Comment on the morphology of the erythrocytes.
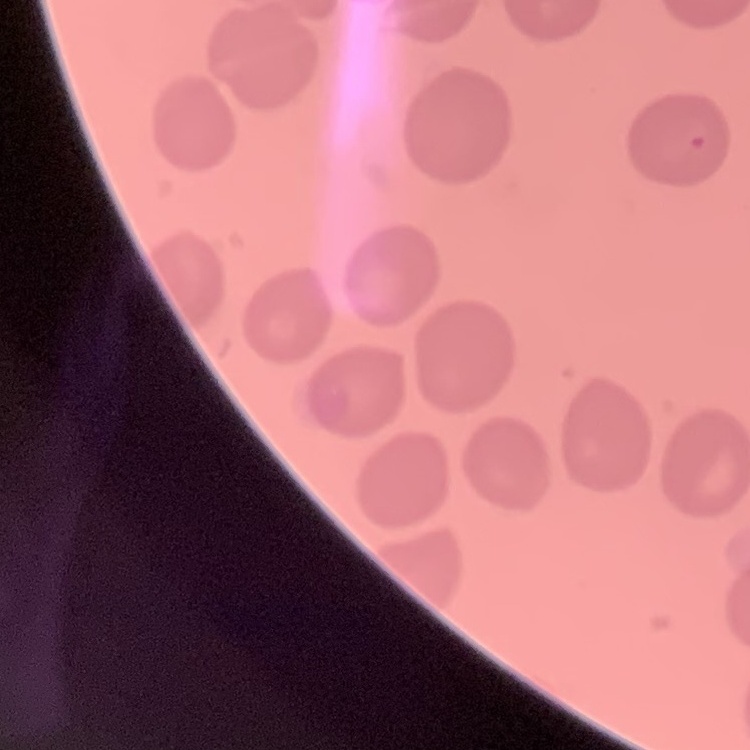

No rouleaux formation.

Summary:
  - Preparation: thin peripheral smear
  - Image type: one tile cut from a larger photomicrograph
  - Stain: Field's or Giemsa